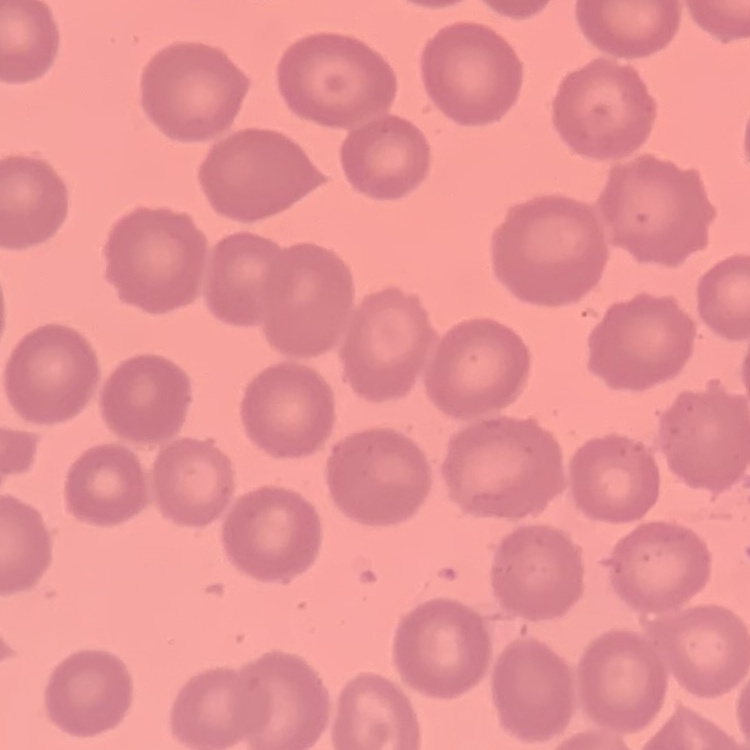

Summary:
  - Red blood cell morphology: no rouleaux formation
  - Stain: Field's or Giemsa
  - Image type: one tile cut from a larger photomicrograph
  - Preparation: thin peripheral smear